Classify this cell by malaria status.
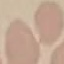

It is uninfected.

Photographed with a smartphone camera at the microscope eyepiece. Thin blood smear. Giemsa stain. Cell patch, automatically extracted from a larger field of view and resized to 64 × 64 pixels.